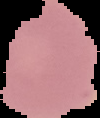
Summary:
  - Image type: cell region segmented out of the field of view; surrounding area masked to black
  - Malaria status: uninfected
  - Preparation: thin blood smear
  - Image size: 100×118 pixels